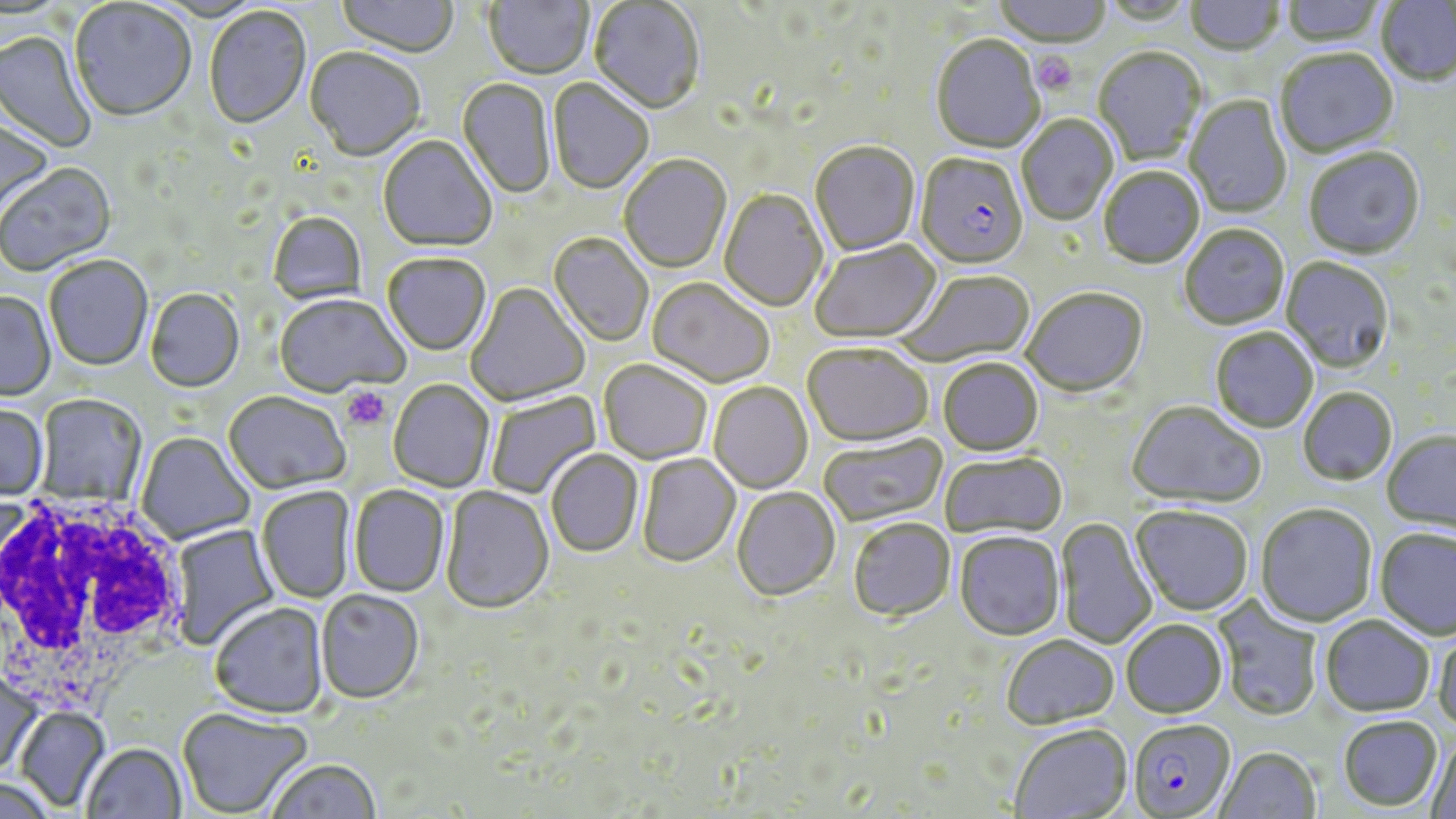
Approximate bounding boxes as [x1, y1, x2, y2] in pixels. Uninfected red blood cell locations: [483, 0, 592, 81], [993, 0, 1112, 49], [1280, 0, 1387, 48], [1375, 0, 1456, 88], [336, 1, 459, 60], [589, 1, 705, 116], [1099, 1, 1196, 27], [1185, 1, 1285, 57], [70, 2, 196, 124], [204, 7, 312, 131], [0, 32, 97, 153], [930, 36, 1045, 155], [1093, 48, 1205, 166], [304, 49, 425, 164], [1275, 50, 1399, 159], [548, 79, 654, 196], [457, 80, 555, 201], [1184, 95, 1292, 219], [0, 115, 52, 224], [1017, 115, 1118, 226], [377, 136, 497, 255], [810, 143, 920, 257], [1304, 149, 1425, 262], [620, 156, 731, 274], [1, 164, 117, 277], [1099, 168, 1205, 271], [719, 189, 828, 313], [268, 213, 367, 305], [1180, 226, 1290, 331], [548, 234, 653, 347], [810, 241, 943, 345], [382, 255, 491, 358], [44, 256, 153, 373], [1281, 258, 1394, 374], [897, 271, 1036, 365], [647, 279, 774, 389], [465, 283, 590, 408], [146, 290, 245, 394], [1022, 290, 1149, 399], [0, 293, 56, 403], [274, 295, 409, 400], [1210, 328, 1318, 434], [802, 344, 932, 449], [938, 359, 1044, 458], [598, 362, 712, 466], [389, 381, 495, 493], [708, 383, 813, 494], [1298, 388, 1397, 487], [486, 390, 602, 499], [224, 394, 349, 496], [37, 396, 145, 506], [1126, 402, 1266, 510], [0, 406, 48, 502], [1382, 432, 1456, 536], [137, 433, 255, 545], [819, 433, 948, 527], [546, 451, 643, 558], [940, 452, 1067, 540], [638, 454, 741, 567], [349, 486, 450, 599], [440, 487, 554, 616], [257, 488, 355, 604], [732, 488, 840, 602], [1255, 504, 1377, 627], [1130, 507, 1253, 617], [1057, 517, 1157, 651], [848, 519, 956, 622], [170, 523, 279, 650], [1375, 529, 1456, 641], [954, 533, 1065, 642], [316, 591, 424, 706], [1210, 594, 1323, 722], [210, 604, 329, 720], [1320, 616, 1435, 718], [1121, 620, 1228, 719], [1432, 627, 1456, 734], [1001, 636, 1120, 730], [0, 670, 44, 777], [16, 708, 110, 811], [178, 710, 312, 817], [1338, 716, 1442, 811], [1008, 724, 1133, 818], [1426, 734, 1456, 819], [83, 745, 187, 819], [1213, 746, 1322, 819], [267, 761, 381, 819], [1, 777, 58, 818]. White blood cell locations: [0, 489, 192, 720]. Plasmodium falciparum-infected red blood cell locations: [916, 155, 1029, 272], [1128, 719, 1236, 818]. Platelet locations: [1032, 52, 1077, 95], [342, 386, 391, 431]. Slide-level diagnosis: Plasmodium falciparum. Image is 1456×819 pixels. May-Grünwald-Giemsa stain. One field of a larger specimen. Thin blood film. Captured at 1000x magnification. Light microscopy.